Give the extent of all Plasmodium falciparum-infected red blood cells.
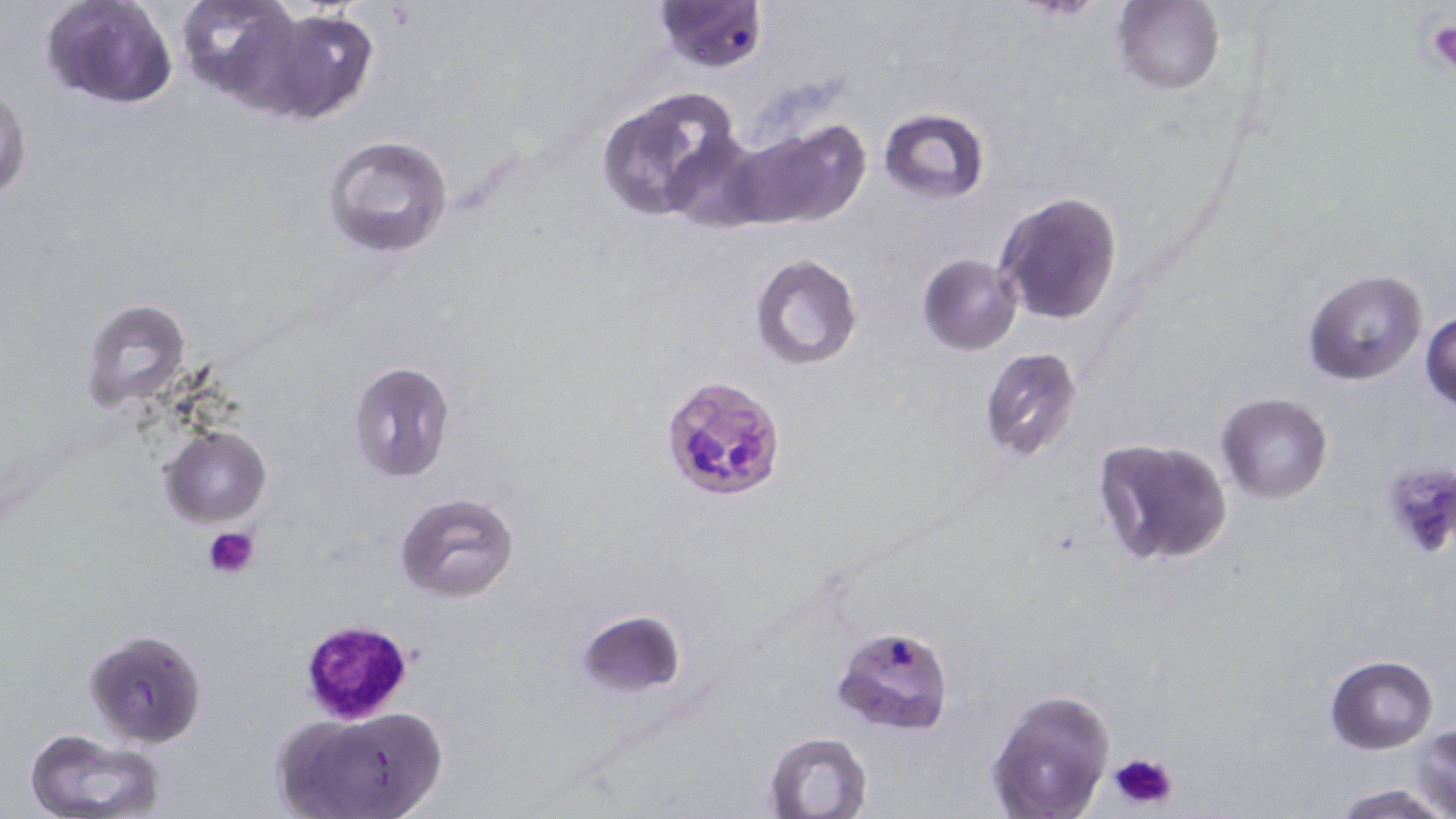

Approximate bounding boxes as [x1, y1, x2, y2] in pixels.
Plasmodium falciparum-infected red blood cells: [652, 0, 767, 72], [659, 374, 791, 506], [831, 624, 954, 734].

{
  "slide_level_diagnosis": "Plasmodium falciparum",
  "uninfected_red_blood_cell_locations": "approximate bounding boxes as [x1, y1, x2, y2] in pixels: [41, 0, 178, 111], [174, 0, 308, 108], [1115, 1, 1223, 95], [260, 9, 380, 122], [0, 84, 31, 204], [595, 91, 740, 221], [877, 107, 990, 203], [731, 120, 871, 231], [664, 131, 770, 231], [324, 135, 454, 257], [994, 191, 1124, 326], [916, 253, 1022, 356], [749, 254, 864, 371], [1304, 270, 1428, 386], [81, 299, 192, 413], [1421, 311, 1455, 412], [979, 347, 1084, 463], [347, 359, 456, 484], [1215, 392, 1333, 502], [158, 424, 271, 527], [1092, 436, 1234, 569], [1379, 460, 1456, 560], [395, 492, 520, 602], [575, 609, 686, 697], [83, 629, 207, 748], [1325, 654, 1439, 754], [984, 688, 1115, 819], [272, 705, 449, 819], [1409, 726, 1455, 815], [23, 728, 169, 819], [764, 731, 873, 817], [1328, 781, 1453, 819]",
  "image_size": "1456×819 pixels",
  "magnification": "1000x",
  "modality": "optical microscopy",
  "platelet_locations": "approximate bounding boxes as [x1, y1, x2, y2] in pixels: [1423, 15, 1456, 72], [204, 525, 259, 579], [298, 619, 415, 722], [1108, 751, 1179, 812]",
  "stain": "May-Grünwald-Giemsa",
  "preparation": "thin blood smear",
  "field_of_view": "single"
}